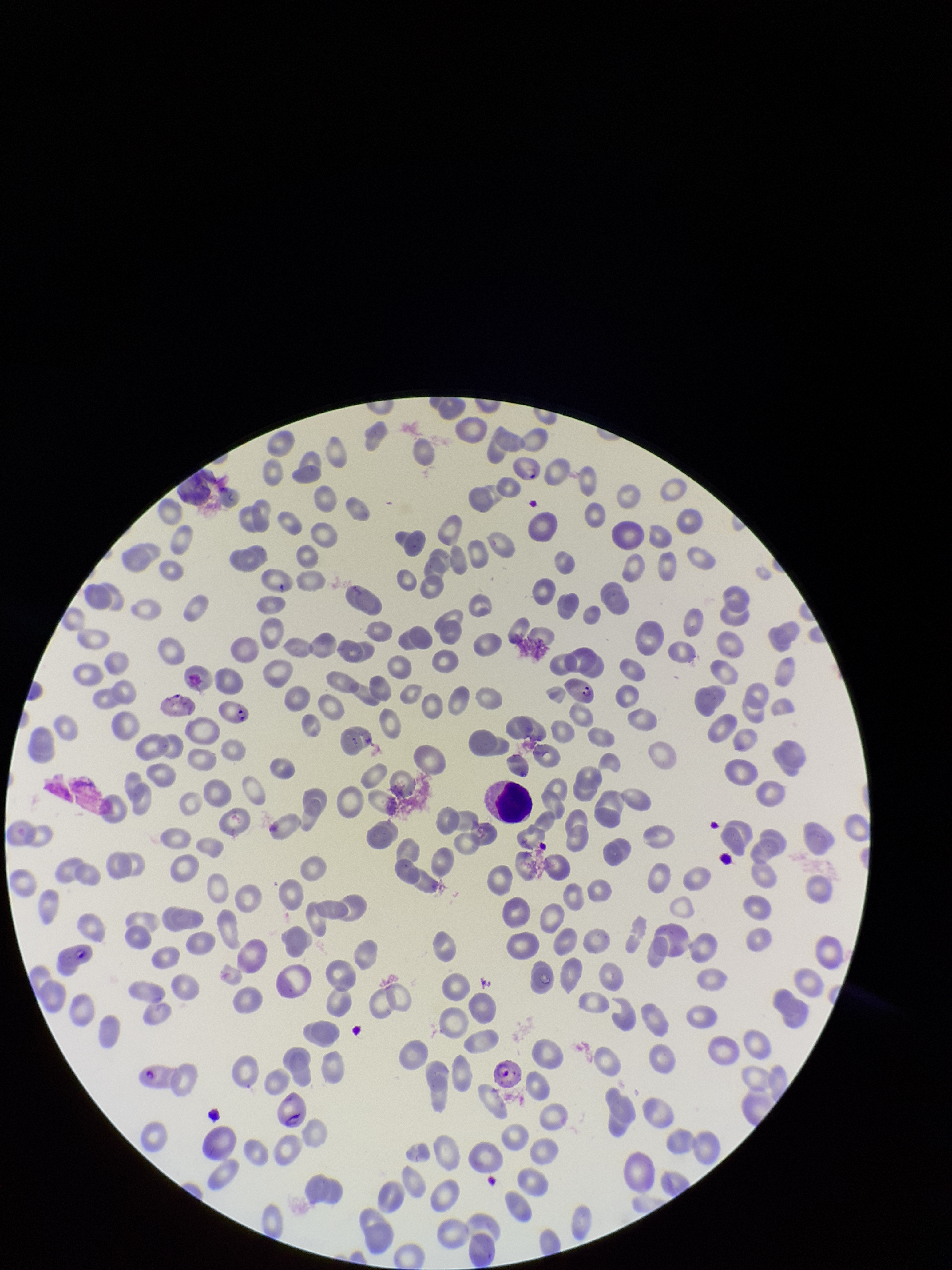
One field from this slide. Photographed through the microscope eyepiece with a smartphone camera. Image is 952×1270 pixels. Patient malaria status: positive. Parasitized red blood cells: detected. Species reported for this patient: Plasmodium falciparum. Parasitized red blood cell count: 5. Preparation: thin. Giemsa stain. Red blood cell count: 257.